Report the malaria status of this cell.
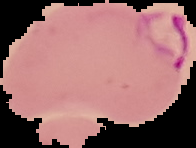
It is parasitized.

Summary:
  - Image size: 196×148 pixels
  - Image type: cell region segmented out of the field of view; surrounding area masked to black
  - Preparation: thin blood film